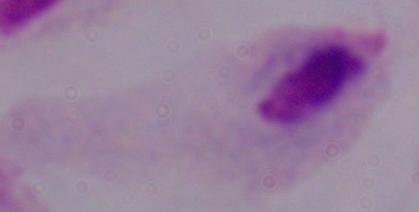

Summary:
  - Modality: photomicrograph
  - Identification: trichomonad
  - Magnification: 1000x